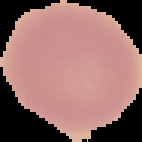

Summary:
  - Result: no Plasmodium parasites seen
  - Image type: cell region segmented out of the field of view; surrounding area masked to black
  - Preparation: thin blood smear
  - Image size: 142×142 pixels